Report the malaria status of this cell.
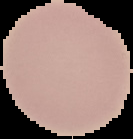
Uninfected.

preparation = thin blood smear
image size = 133×139 pixels
image type = segmented cell region with the area outside set to black